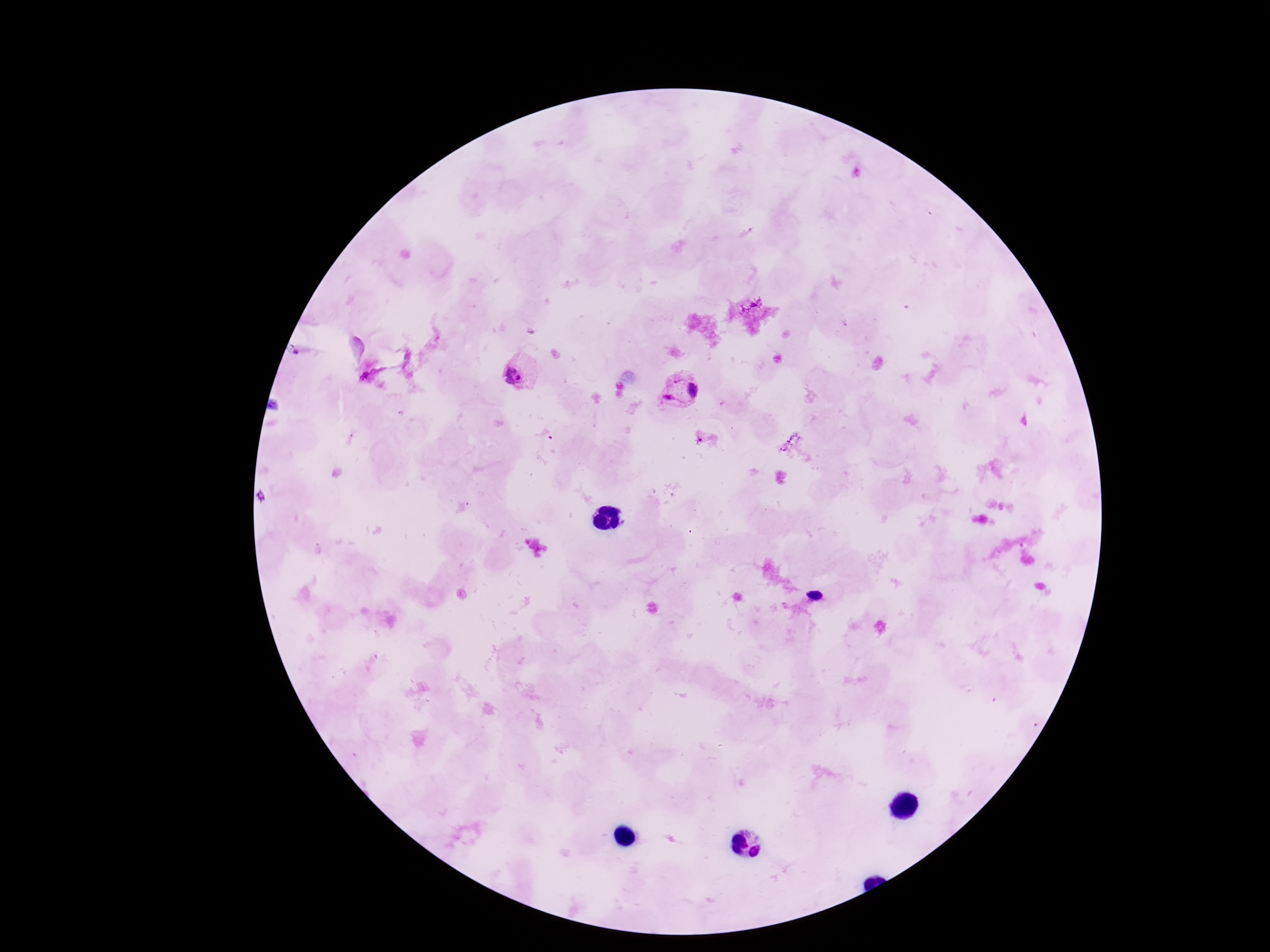
Approximate centers as [x, y] in pixels.
Summary:
  - Plasmodium parasite locations: [517, 371], [684, 391]
  - Magnification: 100x
  - Field of view: single
  - Stain: Giemsa
  - Capture: smartphone camera through the microscope eyepiece
  - Image size: 1270×952 pixels
  - Preparation: thick blood film
  - Patient malaria status: infected